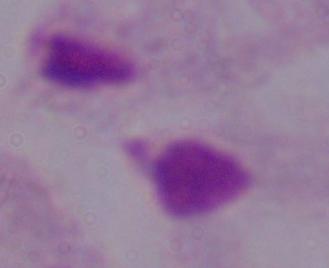

1000x magnification. Photomicrograph. A trichomonad is shown.